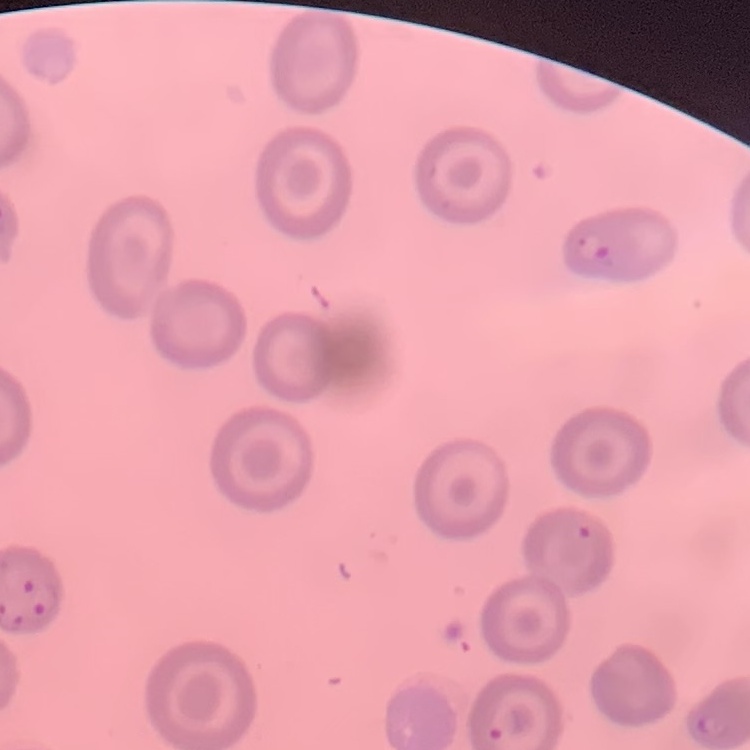
Summary:
  - Erythrocyte morphology: no rouleaux formation
  - Stain: Field's or Giemsa
  - Image type: square crop of a larger photomicrograph
  - Preparation: thin blood smear